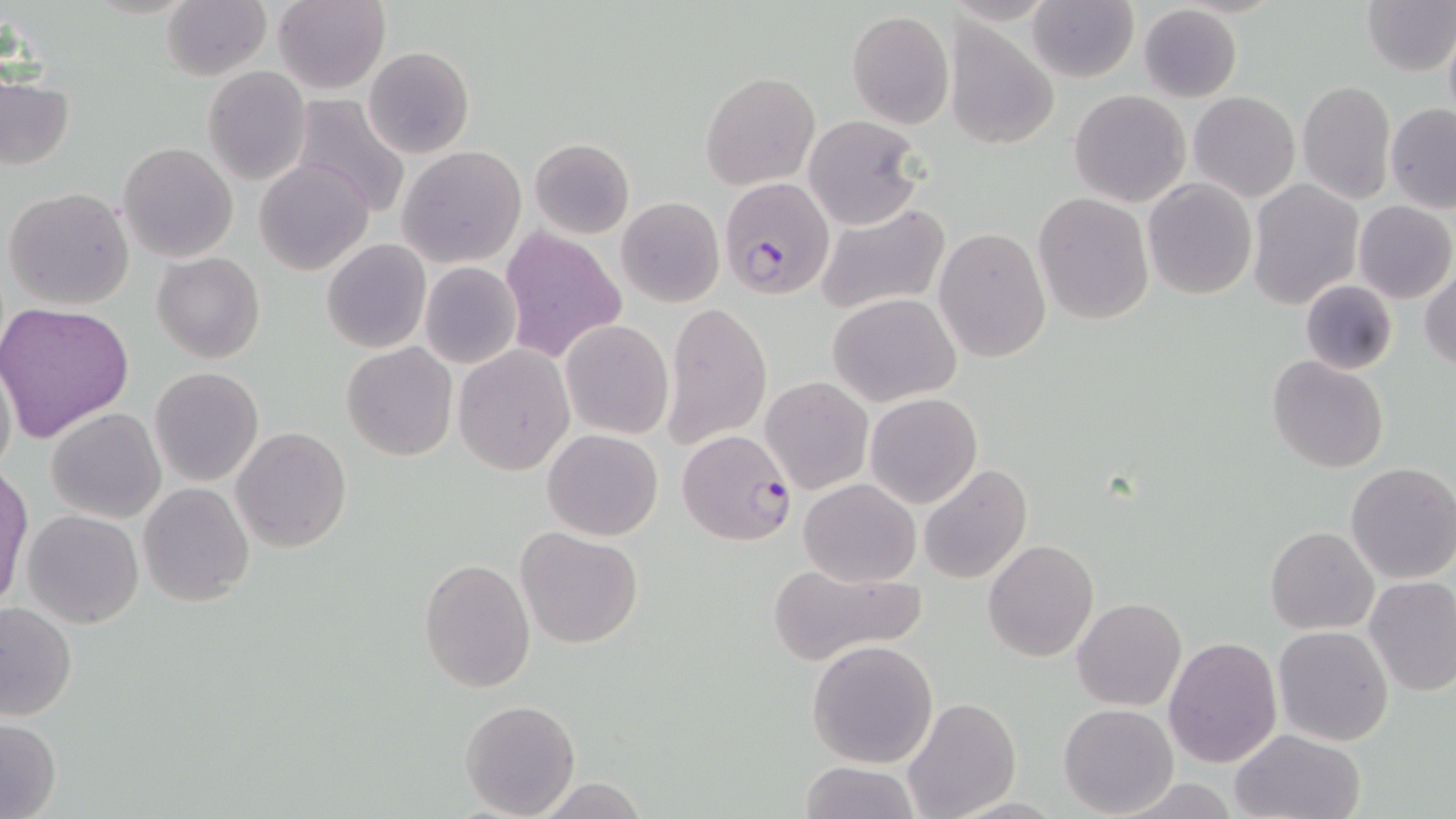

Summary:
  - Coordinate format: approximate bounding boxes as [x1, y1, x2, y2] in pixels
  - Plasmodium falciparum-infected red blood cell locations: [718, 177, 834, 299], [671, 426, 791, 544]
  - Uninfected red blood cell locations: [161, 0, 271, 81], [1361, 0, 1455, 74], [272, 1, 390, 94], [1028, 2, 1137, 82], [1137, 4, 1242, 102], [847, 10, 954, 127], [944, 21, 1051, 150], [1442, 24, 1456, 130], [363, 46, 474, 158], [322, 65, 439, 193], [204, 66, 311, 186], [700, 71, 819, 189], [0, 76, 76, 171], [1296, 78, 1396, 206], [1070, 90, 1190, 207], [1189, 91, 1300, 202], [290, 95, 412, 215], [1385, 103, 1456, 213], [804, 114, 926, 229], [527, 138, 635, 239], [118, 142, 238, 263], [397, 147, 526, 267], [255, 159, 374, 276], [1143, 178, 1257, 300], [1247, 180, 1363, 309], [3, 186, 136, 311], [1032, 192, 1155, 326], [616, 196, 724, 307], [813, 201, 950, 318], [1353, 201, 1455, 302], [500, 227, 627, 362], [934, 227, 1050, 362], [322, 240, 430, 353], [152, 252, 265, 362], [419, 261, 522, 370], [1420, 265, 1455, 372], [1300, 280, 1398, 376], [827, 292, 963, 406], [0, 300, 135, 441], [663, 301, 771, 448], [560, 320, 674, 439], [342, 342, 457, 461], [453, 345, 575, 475], [0, 351, 17, 486], [1266, 356, 1388, 474], [149, 367, 263, 485], [760, 376, 873, 494], [865, 392, 982, 508], [47, 408, 166, 524], [232, 426, 351, 553], [543, 428, 663, 540], [1346, 462, 1456, 584], [918, 464, 1033, 584], [1, 467, 32, 610], [798, 478, 921, 586], [138, 481, 254, 605], [22, 509, 144, 627], [1266, 526, 1378, 634], [515, 527, 643, 649], [983, 538, 1100, 662], [419, 557, 536, 691], [771, 563, 922, 664], [1364, 576, 1456, 696], [1073, 598, 1186, 712], [0, 601, 77, 722], [1272, 625, 1394, 747], [1163, 636, 1282, 767], [807, 638, 939, 769], [900, 698, 1021, 819], [459, 699, 580, 818], [1060, 704, 1179, 816], [0, 716, 61, 818], [1229, 728, 1365, 819], [798, 760, 921, 818], [531, 776, 650, 818], [1110, 777, 1245, 817]
  - Slide-level diagnosis: Plasmodium falciparum
  - Image size: 1456×819 pixels
  - Stain: May-Grünwald-Giemsa
  - Modality: light microscopy
  - Field of view: one of a larger specimen
  - Magnification: 1000x
  - Preparation: thin blood smear